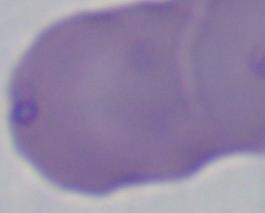

identification: Babesia
modality: micrograph
magnification: 1000x